Assess this cell for malaria.
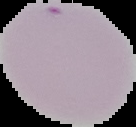

Uninfected.

Summary:
  - Image size: 136×127 pixels
  - Preparation: thin blood film
  - Image type: segmented cell region on a black background